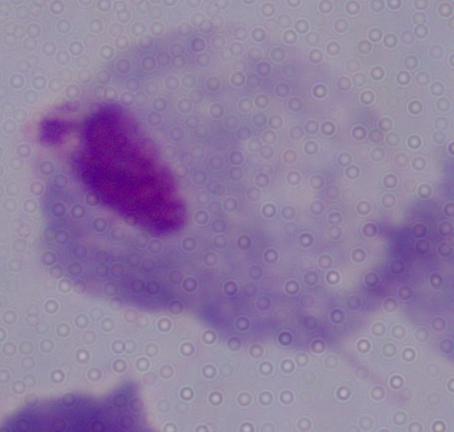

1000x magnification. Micrograph. A trichomonad is seen.